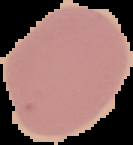

preparation: thin blood film
image_type: cell region segmented out of the field of view; surrounding area masked to black
image_size: 133×145 pixels
result: no Plasmodium parasites detected